Assess the morphology of the red blood cells.
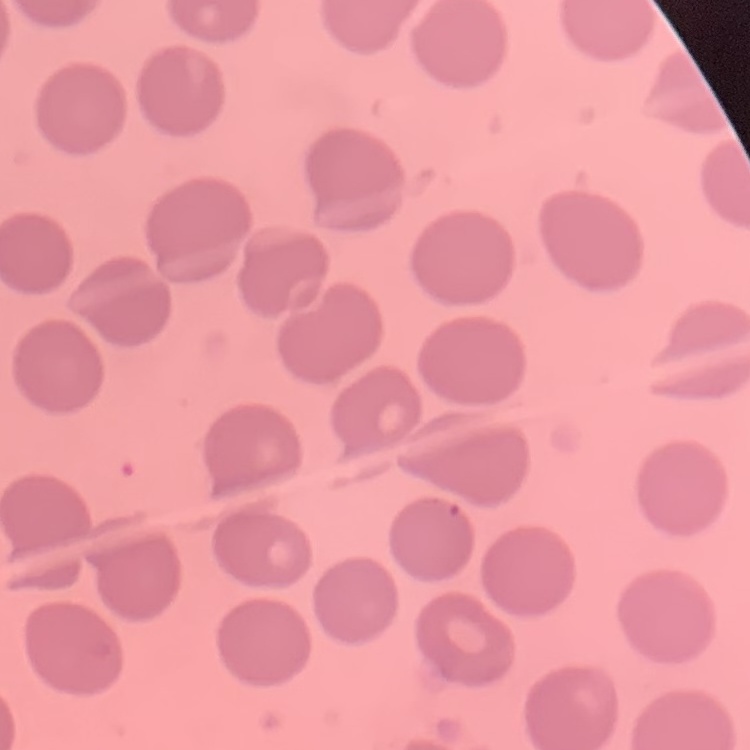

No rouleaux formation.

Stained with either Field's or Giemsa. One tile cut from a larger photomicrograph. Thin blood smear.